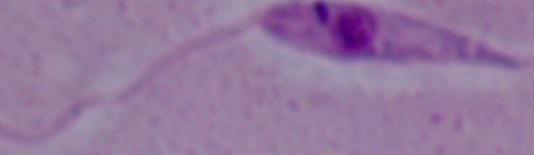

Summary:
  - Modality: photomicrograph
  - Magnification: 1000x
  - Identification: Leishmania